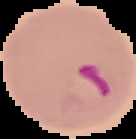
The area outside the segmented cell region is set to black. Malaria status: parasitized. From a thin blood film. Image is 136×139 pixels.